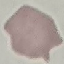

malaria status = uninfected
capture = smartphone camera at the microscope eyepiece
preparation = thin blood film
stain = Giemsa
image type = cell patch, automatically extracted from a larger field of view and resized to 64 × 64 pixels